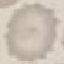
{
  "result": "negative for malaria parasites",
  "image_type": "automatically extracted cell patch, resized to 64 × 64 pixels",
  "capture": "smartphone camera at the microscope eyepiece",
  "preparation": "thin smear",
  "stain": "Giemsa"
}